Identify the cell.
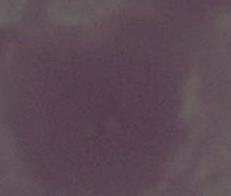

This is an erythrocyte.

Captured at 1000x magnification. Photomicrograph.